Locate every Plasmodium parasite.
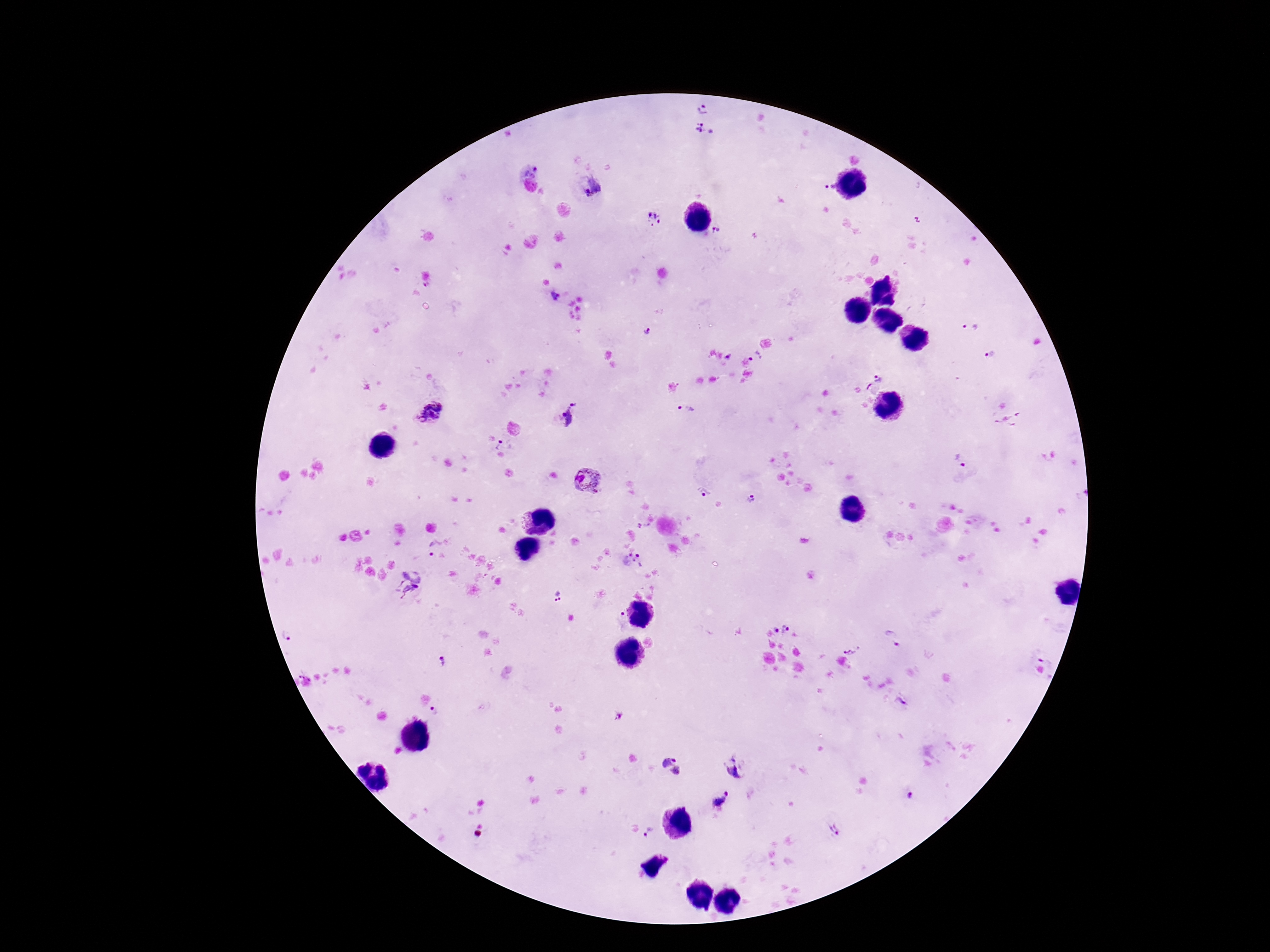
Approximate centers as (x, y) in pixels.
Plasmodium parasites: (702, 109), (704, 129), (536, 169), (592, 186), (827, 186), (653, 219), (718, 230), (556, 297), (969, 328), (647, 331), (989, 354), (756, 356), (728, 357), (878, 377), (868, 387), (685, 411), (430, 414), (570, 416), (1008, 421), (503, 445), (960, 459), (587, 482), (701, 492), (752, 500), (431, 548), (639, 555), (410, 584), (558, 596), (787, 629), (775, 630), (287, 637), (893, 637), (851, 649), (442, 662), (434, 711), (618, 715), (671, 766), (734, 768), (911, 796), (722, 798), (649, 830), (835, 830).

field of view = one from this slide
preparation = thick blood film
stain = Giemsa
magnification = 100x
image size = 1270×952 pixels
capture = smartphone camera through the microscope eyepiece
patient malaria status = infected